Point out every malaria parasite.
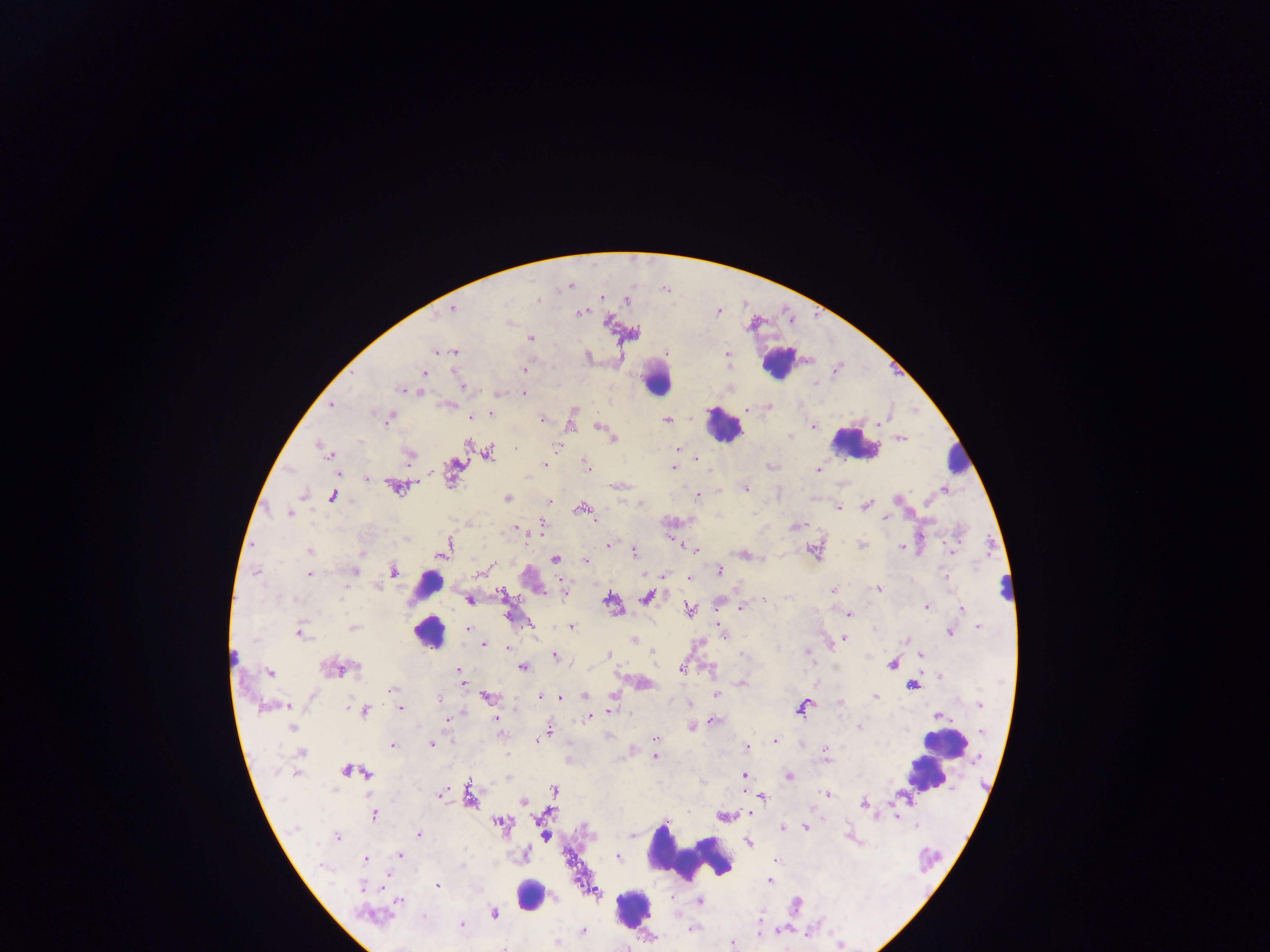

Approximate centers as {x, y} in pixels.
Malaria parasites: {570, 287}, {601, 298}, {537, 299}, {601, 302}, {629, 303}, {455, 307}, {577, 313}, {608, 321}, {749, 328}, {531, 338}, {433, 352}, {452, 353}, {726, 353}, {589, 356}, {423, 372}, {526, 372}, {400, 389}, {419, 392}, {525, 394}, {330, 407}, {768, 408}, {749, 409}, {915, 411}, {574, 413}, {470, 416}, {667, 418}, {388, 420}, {542, 420}, {886, 421}, {572, 423}, {884, 423}, {598, 426}, {814, 426}, {790, 436}, {613, 439}, {900, 439}, {556, 447}, {674, 448}, {695, 457}, {585, 463}, {544, 464}, {407, 465}, {587, 467}, {673, 467}, {817, 470}, {367, 480}, {414, 483}, {615, 486}, {745, 488}, {946, 489}, {697, 497}, {506, 498}, {867, 505}, {837, 507}, {580, 508}, {576, 511}, {288, 514}, {596, 519}, {886, 520}, {543, 522}, {794, 526}, {517, 527}, {527, 536}, {404, 537}, {863, 544}, {607, 545}, {681, 546}, {901, 547}, {695, 549}, {951, 549}, {632, 550}, {446, 551}, {361, 552}, {749, 556}, {585, 560}, {718, 570}, {310, 571}, {393, 572}, {257, 573}, {481, 573}, {948, 576}, {687, 577}, {377, 585}, {565, 587}, {877, 588}, {500, 591}, {832, 591}, {342, 599}, {765, 599}, {470, 600}, {742, 607}, {926, 608}, {962, 609}, {690, 610}, {507, 612}, {847, 614}, {573, 626}, {353, 628}, {978, 628}, {468, 629}, {949, 631}, {301, 632}, {534, 632}, {725, 638}, {845, 639}, {904, 639}, {635, 640}, {484, 646}, {506, 647}, {805, 653}, {652, 654}, {553, 655}, {609, 655}, {922, 656}, {655, 657}, {233, 658}, {523, 667}, {712, 668}, {457, 670}, {681, 670}, {270, 673}, {938, 677}, {643, 684}, {741, 685}, {392, 689}, {615, 693}, {541, 694}, {585, 695}, {718, 695}, {486, 696}, {875, 696}, {561, 698}, {439, 700}, {979, 705}, {289, 706}, {399, 709}, {610, 711}, {595, 716}, {937, 716}, {588, 717}, {496, 719}, {447, 720}, {714, 720}, {692, 727}, {859, 727}, {549, 728}, {654, 739}, {537, 741}, {774, 741}, {393, 743}, {431, 744}, {747, 748}, {827, 751}, {654, 757}, {278, 772}, {297, 773}, {742, 774}, {790, 776}, {829, 794}, {441, 795}, {763, 798}, {863, 805}, {813, 806}, {748, 814}, {373, 817}, {899, 820}, {665, 823}, {915, 826}, {781, 828}, {804, 828}, {417, 834}, {336, 836}, {749, 842}, {400, 854}, {619, 857}, {366, 859}, {323, 866}, {388, 876}, {438, 885}, {361, 888}, {399, 900}, {699, 901}, {387, 915}, {463, 924}, {693, 929}, {732, 941}, {838, 945}, {504, 948}.

Leukocyte locations: {783, 364}, {654, 375}, {725, 422}, {854, 446}, {421, 588}, {429, 634}, {946, 743}, {925, 775}, {690, 855}, {530, 894}, {633, 910}. Single field of view. Mobile-phone photograph taken through the microscope. Thick blood smear. Collected in Ghana. Image is 1270×952 pixels.